Point out every malaria parasite.
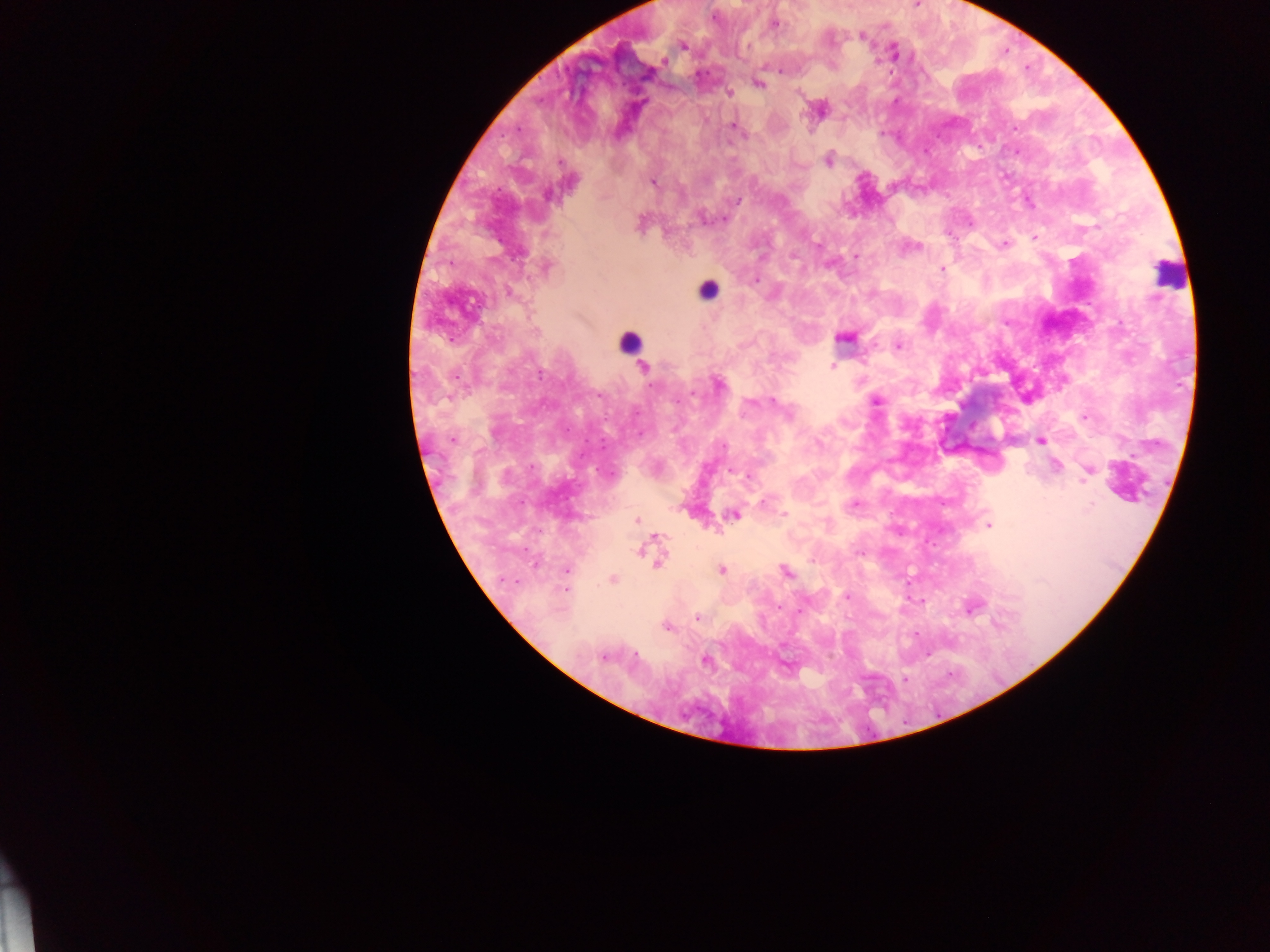

Approximate centers as [x, y] in pixels.
Malaria parasites: [916, 5], [713, 17], [773, 24], [861, 36], [682, 45], [892, 52], [663, 60], [758, 83], [728, 91], [820, 109], [733, 125], [517, 129], [828, 160], [652, 183], [701, 218], [725, 218], [640, 221], [970, 223], [1035, 237], [1003, 243], [910, 246], [855, 258], [545, 266], [942, 269], [755, 280], [508, 291], [844, 337], [897, 345], [833, 366], [643, 368], [717, 383], [876, 400], [773, 401], [789, 416], [1084, 416], [452, 439], [1040, 439], [723, 445], [1055, 466], [1088, 470], [732, 471], [749, 475], [764, 502], [853, 505], [784, 514], [733, 515], [636, 519], [989, 525], [650, 547], [860, 552], [658, 560], [566, 570], [720, 570], [785, 571], [612, 579], [565, 590], [845, 596], [922, 600], [972, 605], [697, 618], [666, 627], [635, 654], [927, 654], [603, 656], [705, 660], [905, 679].

Leukocyte locations: [1169, 273], [707, 289], [629, 342]. One field of view. Thick blood smear. Image is 1270×952 pixels. Sample from Ghana. Photographed through a microscope with a mobile-phone camera.